Report the malaria status of this cell.
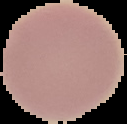
It is uninfected.

image size = 127×124 pixels
image type = segmented cell region with the area outside set to black
preparation = thin blood film